Report the malaria status of this cell.
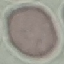
It is uninfected.

Giemsa-stained preparation. Thin blood film. Cell patch, automatically extracted from a larger field of view and resized to 64 × 64 pixels. Photographed with a smartphone camera at the microscope eyepiece.